Assess the morphology of the erythrocytes.
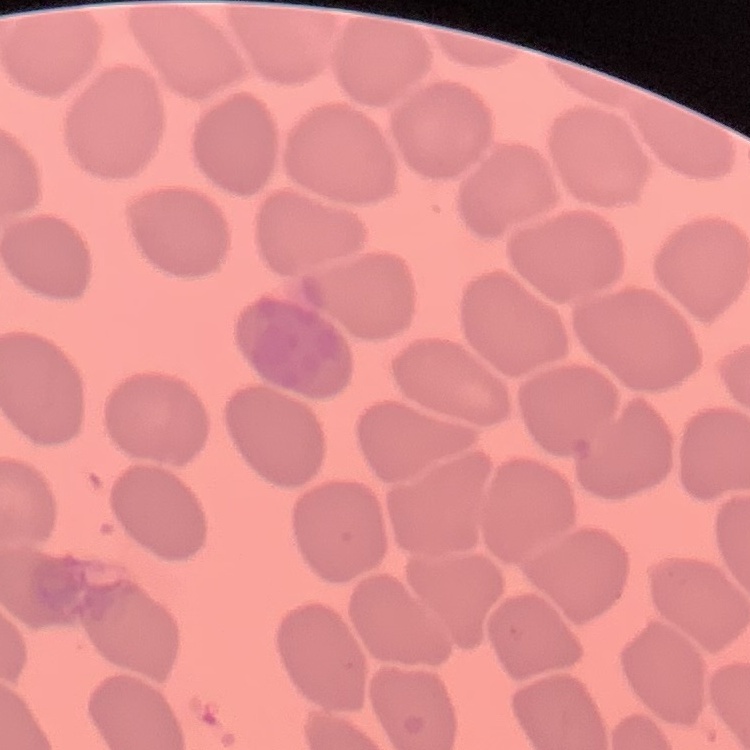

No rouleaux formation.

Summary:
  - Preparation: thin blood smear
  - Stain: Field's or Giemsa
  - Image type: one tile cut from a larger photomicrograph